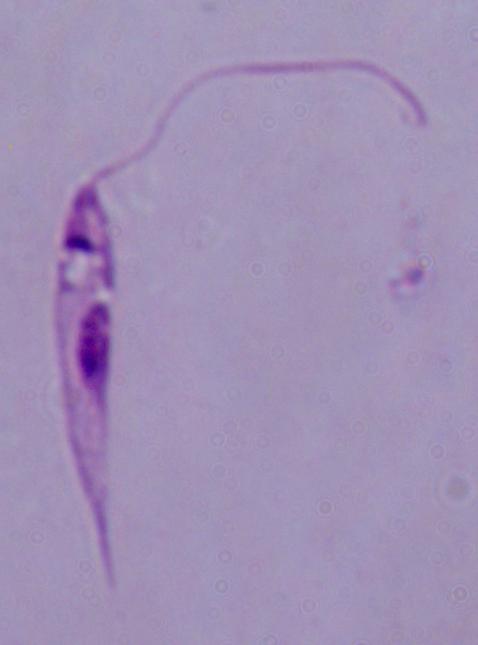
A Leishmania parasite is shown. Photomicrograph. 1000x magnification.